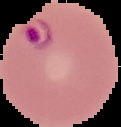

The area outside the segmented cell region is set to black. Malaria status: parasitized. Image is 121×127 pixels. From a thin blood smear.